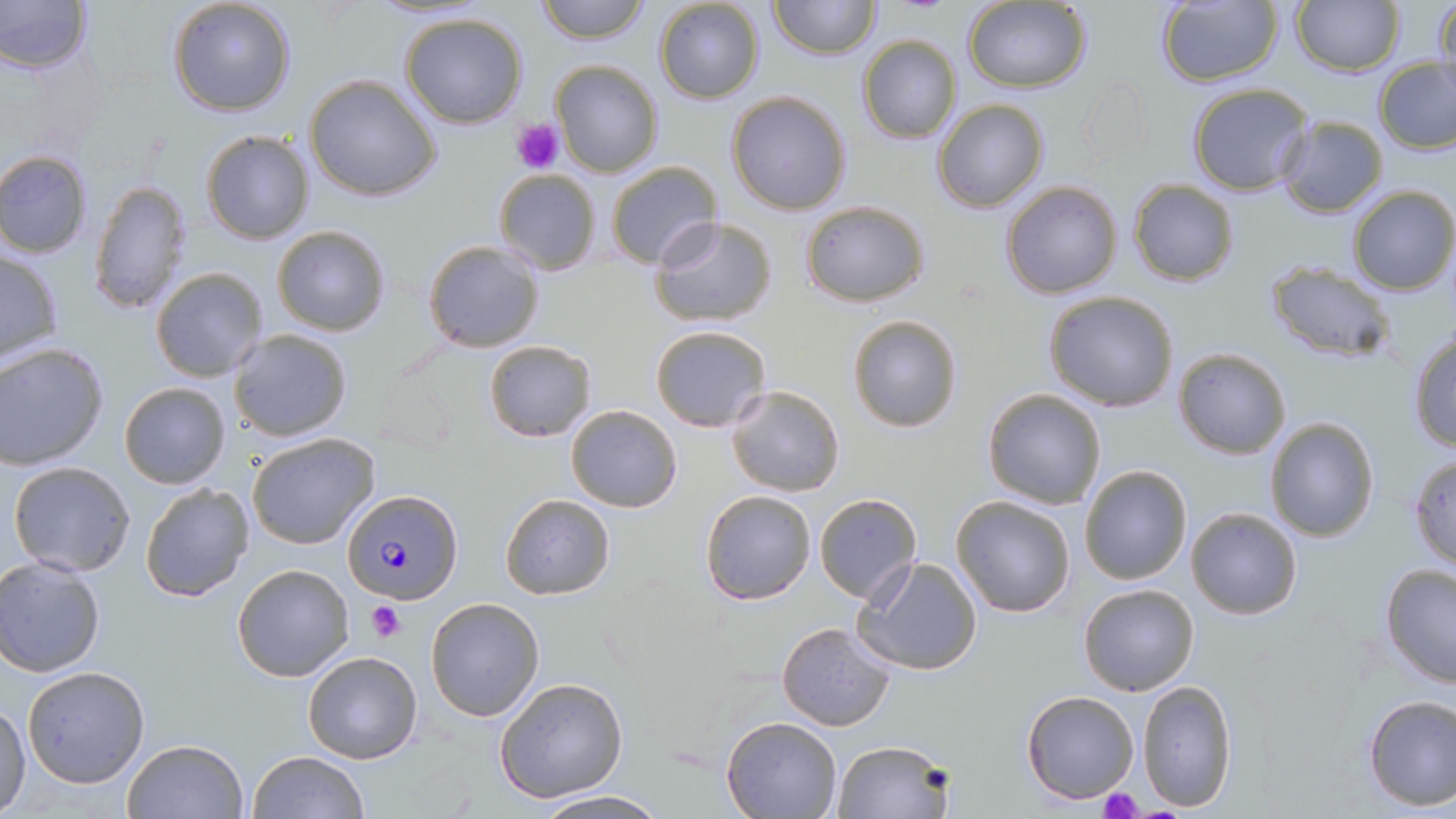
Summary:
  - Coordinate format: approximate bounding boxes as (x1, y1, x2, y2) in pixels
  - Uninfected red blood cell locations: (0, 0, 93, 74), (167, 0, 297, 118), (533, 0, 652, 45), (770, 0, 879, 60), (1433, 0, 1456, 93), (653, 1, 766, 104), (1155, 1, 1282, 87), (1292, 1, 1403, 75), (964, 2, 1092, 94), (397, 12, 530, 129), (857, 34, 962, 144), (1373, 55, 1456, 154), (549, 60, 663, 177), (304, 74, 442, 203), (1081, 75, 1154, 165), (1188, 83, 1313, 196), (727, 91, 851, 214), (933, 100, 1049, 214), (1276, 116, 1389, 219), (200, 130, 316, 244), (1, 150, 94, 258), (605, 160, 722, 270), (493, 168, 601, 277), (1127, 178, 1239, 286), (87, 180, 193, 316), (1001, 180, 1123, 299), (1347, 184, 1456, 297), (799, 199, 929, 306), (649, 216, 777, 327), (272, 224, 391, 335), (423, 239, 544, 352), (0, 250, 64, 365), (1266, 264, 1398, 364), (150, 266, 269, 383), (1042, 289, 1180, 413), (847, 315, 962, 433), (650, 325, 771, 432), (1407, 328, 1456, 453), (227, 329, 353, 443), (484, 339, 597, 441), (0, 343, 109, 469), (1172, 348, 1291, 459), (119, 382, 230, 489), (725, 384, 847, 497), (982, 389, 1107, 511), (565, 405, 682, 513), (1264, 417, 1379, 541), (246, 432, 380, 550), (1409, 457, 1456, 571), (7, 460, 137, 577), (1080, 465, 1192, 585), (139, 483, 253, 602), (699, 489, 815, 605), (814, 493, 921, 606), (500, 494, 614, 599), (950, 495, 1077, 619), (1186, 507, 1303, 620), (853, 556, 983, 676), (0, 557, 106, 677), (1380, 563, 1456, 689), (231, 565, 354, 682), (1077, 581, 1200, 696), (424, 597, 544, 721), (776, 623, 895, 731), (301, 650, 424, 765), (22, 665, 150, 788), (494, 677, 627, 803), (1136, 679, 1238, 811), (1021, 690, 1141, 804), (1361, 694, 1455, 812), (0, 701, 31, 814), (721, 716, 842, 818), (122, 737, 250, 819), (832, 739, 952, 819), (247, 750, 367, 818), (530, 790, 669, 819)
  - Platelet locations: (512, 119, 566, 173), (367, 602, 406, 641), (1100, 788, 1140, 819)
  - Plasmodium falciparum-infected red blood cell locations: (342, 488, 463, 604)
  - Slide-level diagnosis: Plasmodium falciparum
  - Modality: light microscopy
  - Image size: 1456×819 pixels
  - Stain: May-Grünwald-Giemsa
  - Preparation: thin blood film
  - Magnification: 1000x
  - Field of view: single